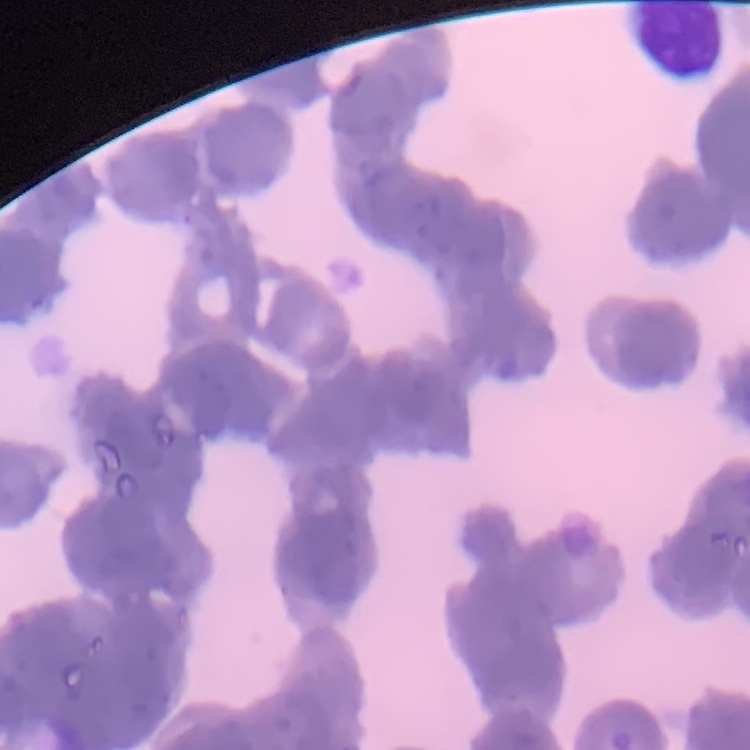

The red blood cells exhibit rouleaux formation. Square crop of a larger photomicrograph. Thin blood smear. Field's or Giemsa stain.